Identify the cell.
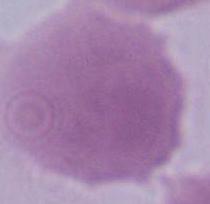

An erythrocyte.

Micrograph. 1000x magnification.